Classify this cell by malaria status.
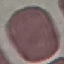

It is uninfected.

Cell patch, automatically extracted from a larger field of view and resized to 64 × 64 pixels. Thin smear of blood. Giemsa-stained preparation. Photographed with a smartphone camera at the microscope eyepiece.